Give the extent of all Plasmodium falciparum-infected red blood cells.
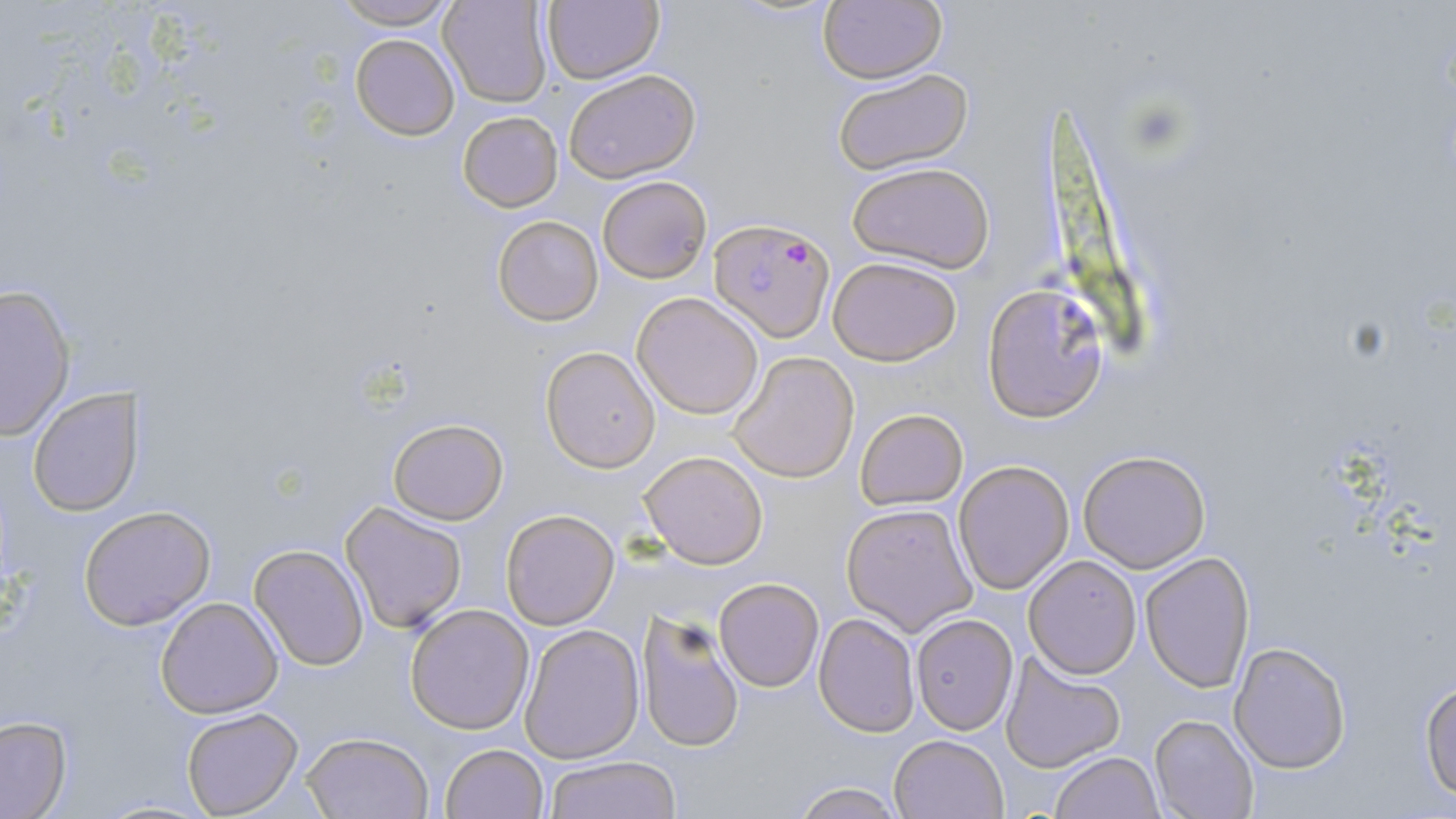
Approximate bounding boxes as [x1, y1, x2, y2] in pixels.
Plasmodium falciparum-infected red blood cells: [710, 217, 833, 341].

slide-level diagnosis = Plasmodium falciparum
magnification = 1000x
field of view = one of a larger specimen
modality = light microscopy
preparation = thin blood smear
stain = May-Grünwald-Giemsa
uninfected red blood cell locations = approximate bounding boxes as [x1, y1, x2, y2] in pixels: [325, 0, 461, 29], [818, 0, 948, 85], [439, 1, 553, 108], [541, 1, 665, 84], [350, 33, 460, 142], [828, 66, 976, 178], [564, 69, 701, 184], [457, 109, 564, 212], [846, 161, 994, 274], [598, 174, 712, 284], [493, 215, 603, 327], [827, 255, 964, 366], [1, 283, 76, 441], [982, 284, 1110, 419], [631, 291, 764, 421], [541, 347, 660, 472], [728, 352, 861, 484], [27, 387, 145, 516], [855, 407, 968, 511], [388, 417, 508, 524], [639, 450, 767, 569], [1079, 450, 1211, 573], [953, 460, 1074, 595], [341, 499, 468, 634], [841, 502, 978, 635], [79, 505, 215, 631], [499, 507, 620, 630], [250, 544, 370, 671], [1139, 550, 1256, 692], [1023, 555, 1142, 679], [714, 576, 824, 692], [156, 596, 282, 718], [405, 603, 535, 734], [637, 606, 746, 755], [912, 612, 1018, 735], [813, 613, 920, 737], [518, 624, 643, 763], [1229, 642, 1352, 773], [999, 649, 1126, 774], [1419, 678, 1456, 802], [181, 708, 302, 816], [1150, 714, 1259, 819], [0, 716, 72, 818], [301, 731, 434, 819], [888, 733, 1009, 819], [440, 743, 548, 819], [1048, 751, 1162, 819], [544, 756, 683, 818], [791, 780, 904, 818]
image size = 1456×819 pixels